Classify this cell by malaria status.
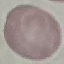

Uninfected.

image type = automatically extracted cell patch, resized to 64 × 64 pixels
capture = smartphone camera at the microscope eyepiece
preparation = thin smear
stain = Giemsa